State which parasite is depicted.
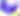

Toxoplasma gondii.

Summary:
  - Magnification: 400x
  - Modality: photomicrograph